State the preparation type.
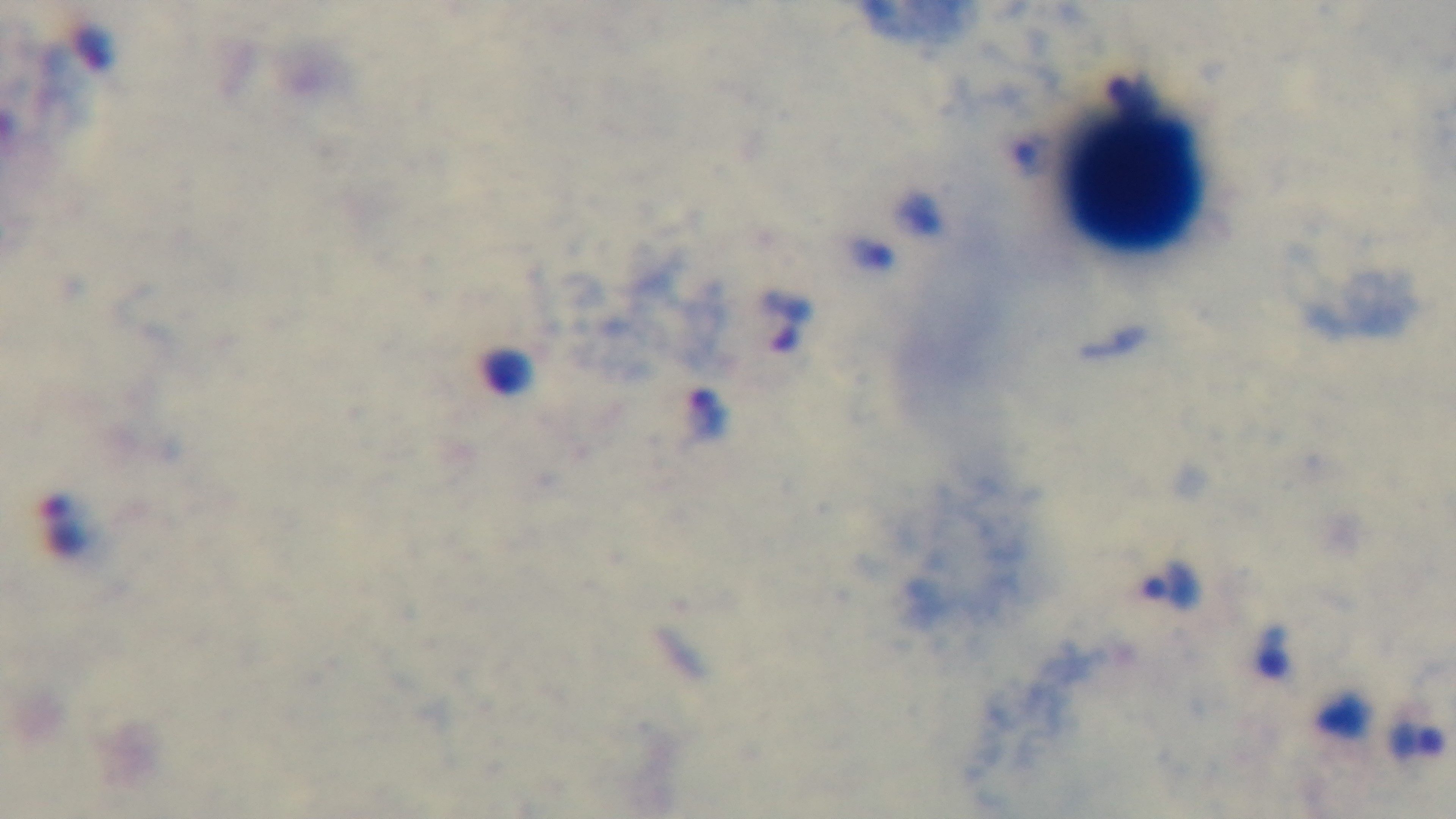
Thick.

{
  "field_of_view": "one from the slide",
  "objective": "100x oil immersion",
  "modality": "light microscopy",
  "malaria_status": "positive",
  "stain": "Giemsa",
  "capture": "mounted 4K digital camera"
}